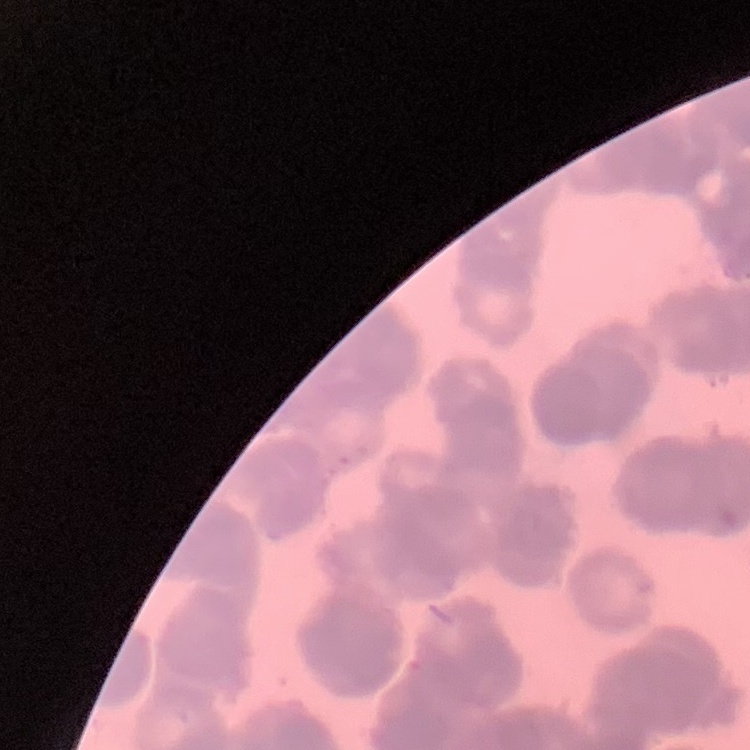
Summary:
  - Red blood cell morphology: rouleaux formation
  - Image type: square crop of a larger photomicrograph
  - Preparation: thin peripheral smear
  - Stain: Field's or Giemsa